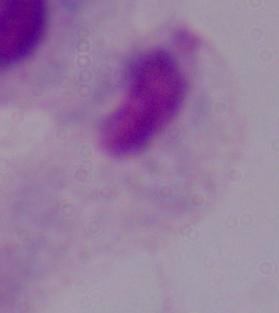
Micrograph. A trichomonad is seen. Captured at 1000x magnification.